Report the malaria status of this cell.
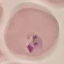

Parasitized.

Acquired by smartphone through the microscope eyepiece. Automatically extracted cell patch, resized to 64 × 64 pixels. Giemsa stain. Thin smear of blood.